Assess this cell for malaria.
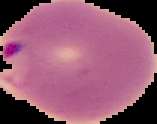

It is parasitized.

Segmented cell region on a black background. From a thin blood smear. Image is 157×124 pixels.